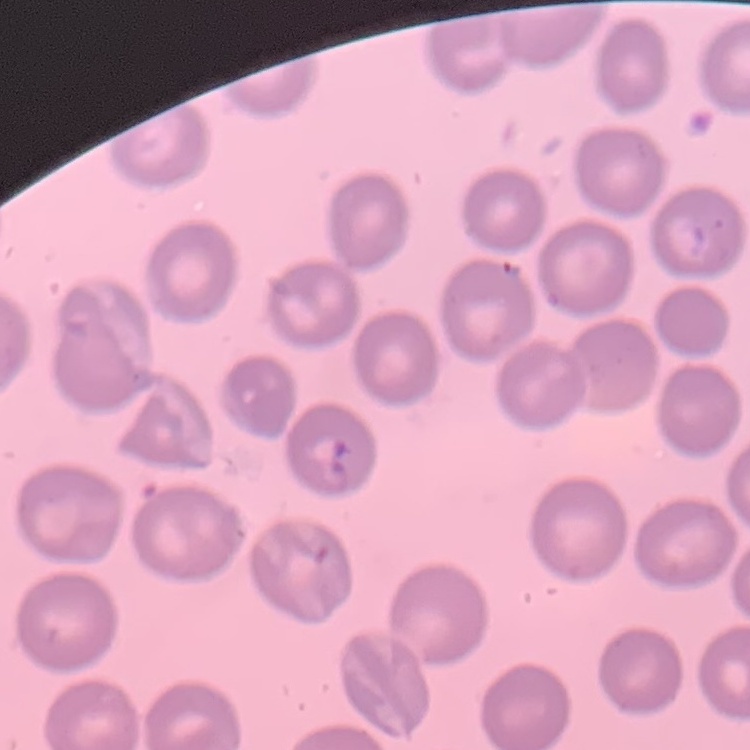
The red blood cells exhibit no rouleaux formation. Thin blood film. One tile cut from a larger photomicrograph. Stained with either Field's or Giemsa.